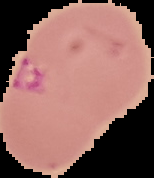

From a thin blood film. Image is 154×178 pixels. Segmented cell region on a black background. Result: Plasmodium parasites detected.